Describe the morphology of the erythrocytes.
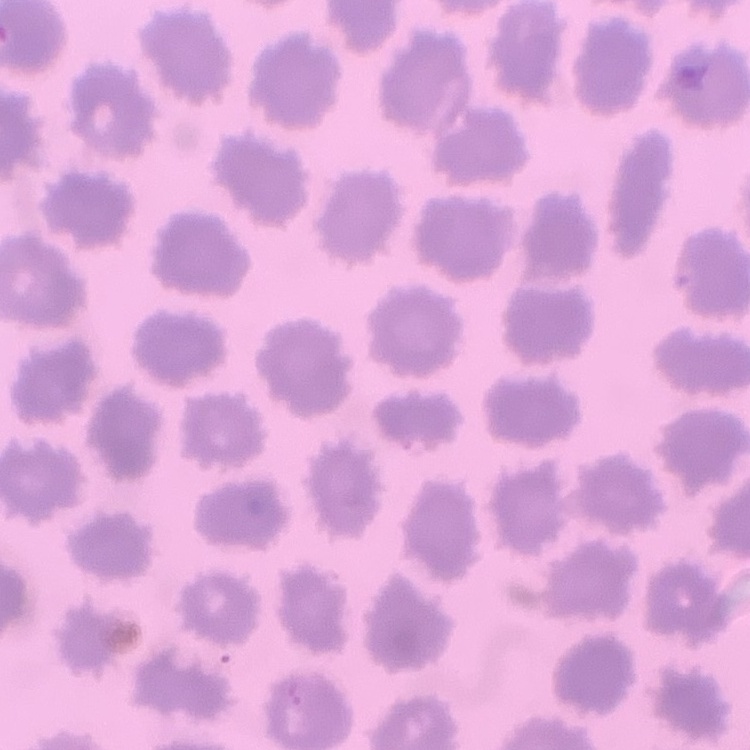
No rouleaux formation.

One tile cut from a larger photomicrograph. Thin peripheral smear. Stained with either Field's or Giemsa.